Describe the morphology of the red blood cells.
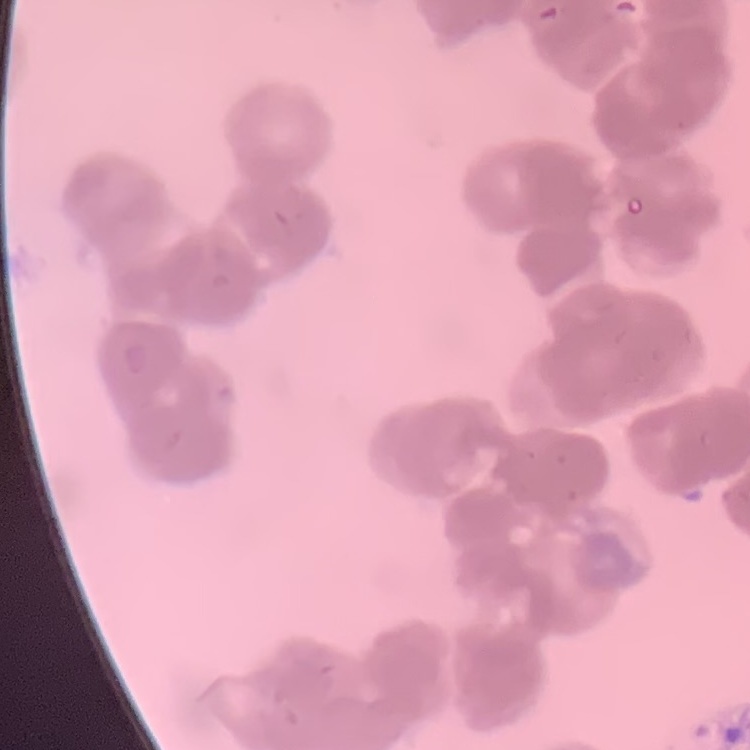

They show rouleaux formation.

stain: Field's or Giemsa
preparation: thin blood film
image_type: one tile cut from a larger photomicrograph